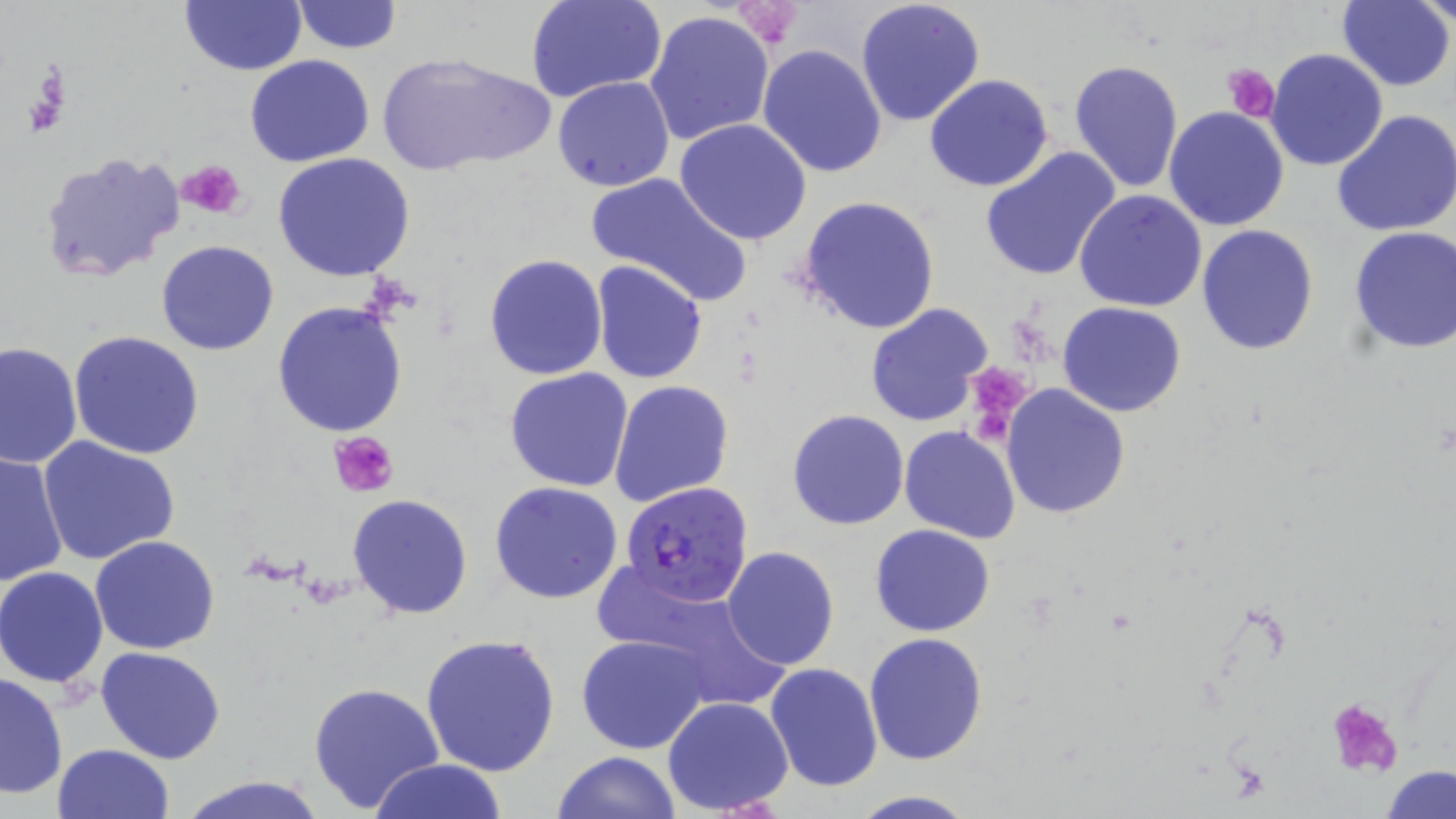
Summary:
  - Coordinate format: approximate bounding boxes as (x1,y1)-(x2,y2) corner pairs in pixels
  - Platelet locations: (729,1)-(804,50), (1224,62)-(1280,122), (23,66)-(69,140), (179,160)-(246,219), (966,364)-(1031,426), (330,431)-(401,499), (1326,695)-(1405,778)
  - Plasmodium falciparum-infected red blood cell locations: (620,481)-(755,606)
  - Uninfected red blood cell locations: (289,0)-(403,53), (527,0)-(665,104), (856,0)-(986,126), (1336,0)-(1454,91), (1419,0)-(1455,30), (179,2)-(307,76), (644,12)-(775,146), (759,43)-(889,178), (1265,48)-(1390,172), (375,52)-(551,177), (244,54)-(374,168), (1067,57)-(1183,196), (923,74)-(1054,191), (552,76)-(676,192), (1164,107)-(1290,230), (1332,109)-(1456,238), (675,119)-(813,245), (979,148)-(1121,283), (38,151)-(185,285), (272,153)-(416,282), (583,171)-(748,305), (1075,190)-(1208,313), (798,196)-(943,336), (1197,224)-(1321,356), (1346,227)-(1456,355), (155,239)-(280,356), (484,253)-(608,380), (590,261)-(709,385), (272,301)-(408,437), (1057,301)-(1187,418), (866,302)-(995,427), (69,332)-(204,461), (1,341)-(82,469), (503,368)-(635,493), (609,382)-(734,507), (1000,383)-(1131,519), (787,409)-(909,530), (899,425)-(1022,546), (37,438)-(181,565), (1,449)-(69,587), (490,482)-(624,604), (347,493)-(475,620), (870,523)-(996,638), (90,535)-(221,656), (722,546)-(840,670), (1,567)-(108,688), (421,633)-(561,777), (864,634)-(987,765), (576,635)-(711,753), (96,645)-(227,764), (765,663)-(884,793), (1,671)-(69,798), (307,681)-(445,815), (663,696)-(794,815), (51,743)-(176,819), (551,752)-(681,819), (367,757)-(509,819), (1381,765)-(1456,819), (175,772)-(330,819), (844,791)-(980,819)
  - Slide-level diagnosis: Plasmodium falciparum
  - Modality: optical microscopy
  - Image size: 1456×819 pixels
  - Field of view: single
  - Magnification: 1000x
  - Stain: May-Grünwald-Giemsa
  - Preparation: thin blood film